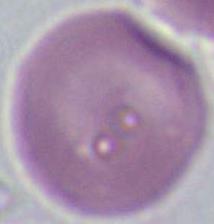

Photomicrograph. Captured at 1000x magnification. An erythrocyte is shown.